Assess the morphology of the red blood cells.
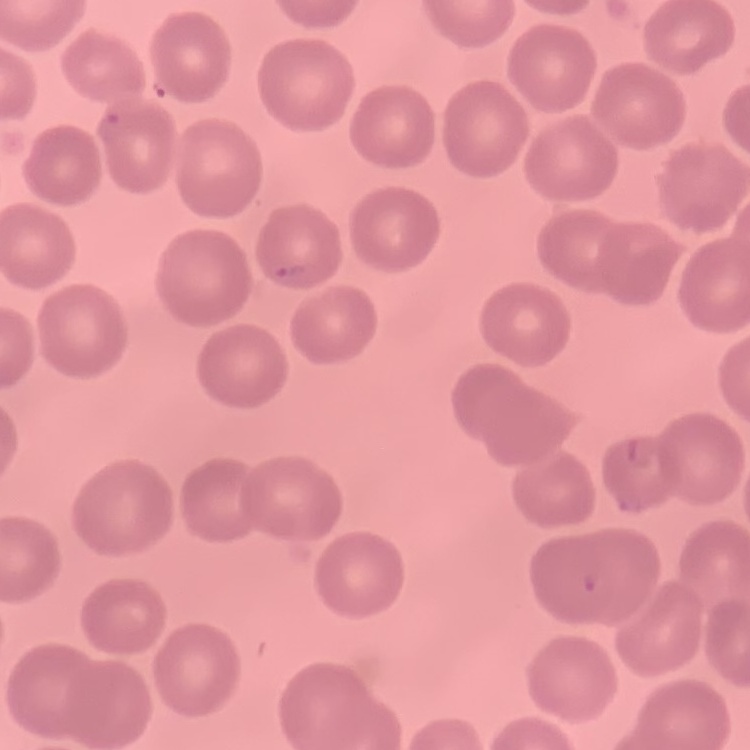

No rouleaux formation.

Summary:
  - Preparation: thin peripheral smear
  - Image type: one tile cut from a larger photomicrograph
  - Stain: Field's or Giemsa